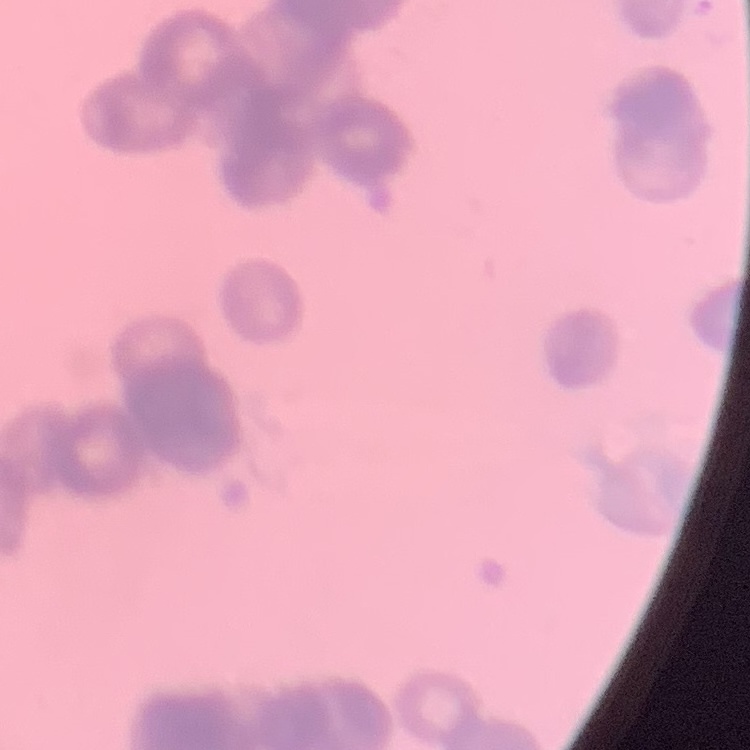
Summary:
  - Erythrocyte morphology: rouleaux formation
  - Image type: one tile cut from a larger photomicrograph
  - Preparation: thin blood film
  - Stain: Field's or Giemsa